Locate every blood parasite and identify its species.
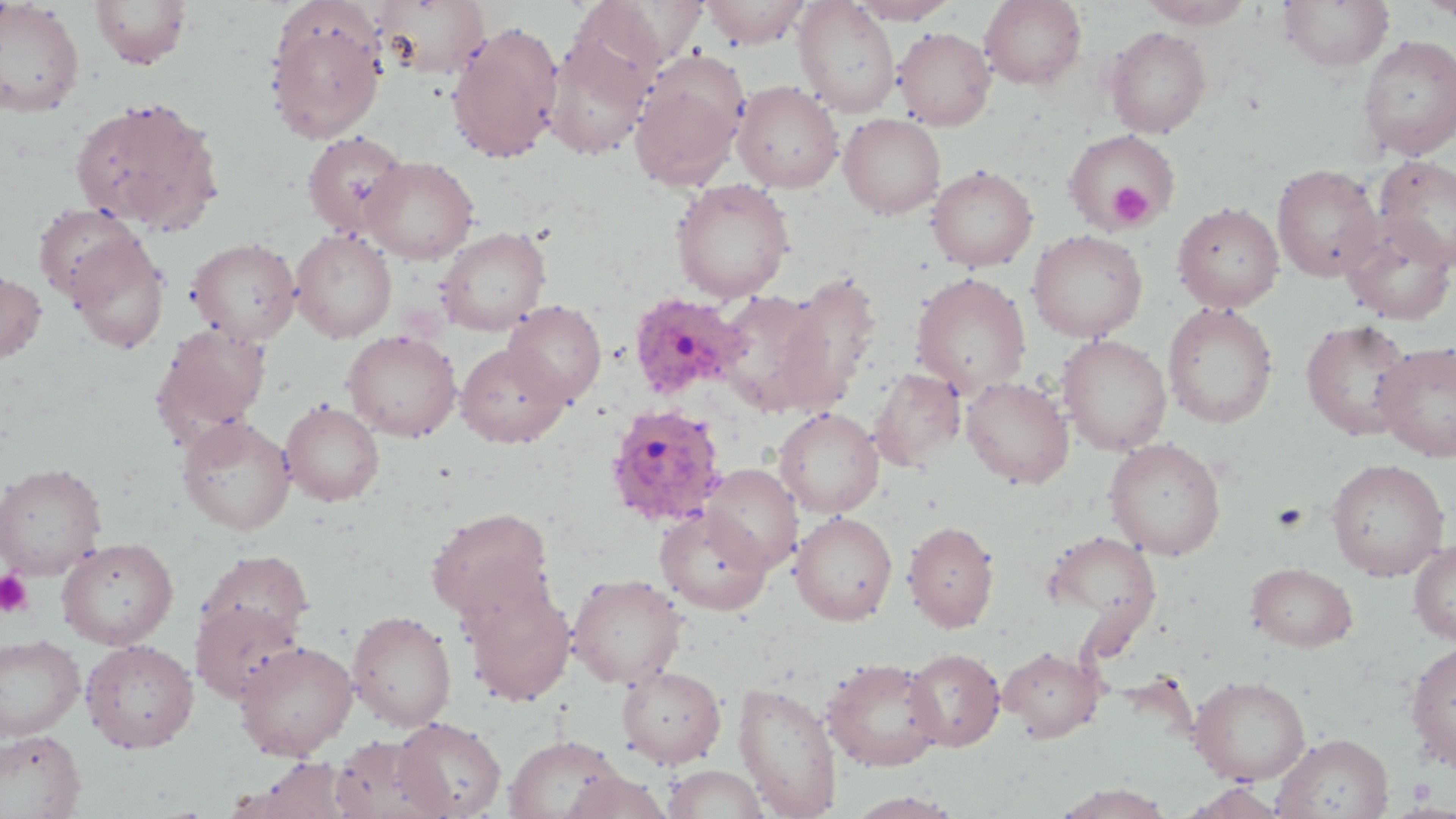
Approximate bounding boxes as (x1, y1, x2, y2) in pixels.
Plasmodium ovale-infected red blood cells: (628, 292, 749, 401), (604, 403, 729, 528).
No Plasmodium falciparum, Plasmodium malariae, Plasmodium vivax, Babesia divergens, or Trypanosoma brucei observed.

{
  "slide_level_diagnosis": "Plasmodium ovale",
  "preparation": "thin blood film",
  "image_size": "1456×819 pixels",
  "magnification": "1000x",
  "platelet_locations": "approximate bounding boxes as (x1, y1, x2, y2) in pixels: (1108, 183, 1152, 227), (0, 571, 33, 617)",
  "field_of_view": "one of a larger specimen",
  "uninfected_red_blood_cell_locations": "approximate bounding boxes as (x1, y1, x2, y2) in pixels: (0, 0, 85, 117), (371, 0, 490, 80), (700, 0, 811, 48), (979, 0, 1087, 90), (1138, 0, 1257, 28), (1278, 0, 1394, 71), (1418, 0, 1456, 21), (90, 1, 192, 69), (589, 1, 710, 67), (794, 1, 900, 117), (848, 1, 959, 24), (266, 11, 386, 144), (447, 22, 564, 163), (1103, 26, 1212, 138), (893, 27, 996, 130), (544, 30, 654, 161), (1357, 35, 1456, 160), (629, 60, 747, 190), (732, 81, 843, 193), (69, 96, 224, 235), (839, 113, 946, 219), (1062, 127, 1181, 233), (302, 131, 410, 238), (1373, 155, 1456, 271), (361, 156, 479, 264), (1272, 163, 1383, 282), (926, 165, 1038, 272), (671, 178, 795, 302), (33, 202, 141, 304), (1172, 202, 1284, 313), (1341, 216, 1455, 325), (436, 227, 551, 336), (290, 229, 397, 343), (1027, 229, 1148, 343), (65, 232, 170, 354), (187, 237, 301, 345), (0, 270, 47, 363), (910, 272, 1032, 396), (774, 274, 881, 412), (715, 289, 834, 413), (502, 300, 606, 406), (1163, 302, 1279, 429), (1299, 318, 1416, 441), (151, 323, 272, 445), (342, 329, 462, 442), (1057, 334, 1172, 456), (1373, 341, 1456, 462), (455, 342, 571, 448), (869, 367, 966, 471), (961, 376, 1074, 489), (280, 400, 385, 506), (774, 407, 884, 518), (178, 415, 296, 536), (1104, 438, 1226, 560), (1326, 458, 1450, 581), (0, 462, 107, 580), (703, 464, 803, 573), (426, 507, 555, 622), (655, 507, 772, 615), (791, 512, 897, 625), (903, 520, 1000, 632), (1042, 530, 1162, 637), (57, 536, 178, 649), (1409, 539, 1456, 646), (198, 550, 313, 646), (1245, 562, 1359, 651), (567, 574, 687, 689), (462, 581, 576, 706), (190, 599, 303, 705), (348, 609, 457, 732), (0, 635, 84, 741), (80, 639, 199, 753), (234, 640, 358, 760), (1404, 641, 1456, 771), (999, 645, 1103, 742), (904, 648, 1006, 751), (821, 657, 945, 772), (616, 665, 726, 768), (1189, 675, 1311, 785), (733, 679, 843, 818), (392, 716, 506, 818), (0, 729, 87, 818), (1272, 733, 1394, 819), (504, 734, 627, 819), (330, 735, 447, 819), (243, 758, 357, 818), (663, 765, 768, 819), (560, 770, 674, 818), (1179, 781, 1290, 819), (1053, 783, 1175, 819), (846, 791, 962, 818)",
  "stain": "May-Grünwald-Giemsa",
  "modality": "light microscopy"
}